Locate and identify every blood parasite.
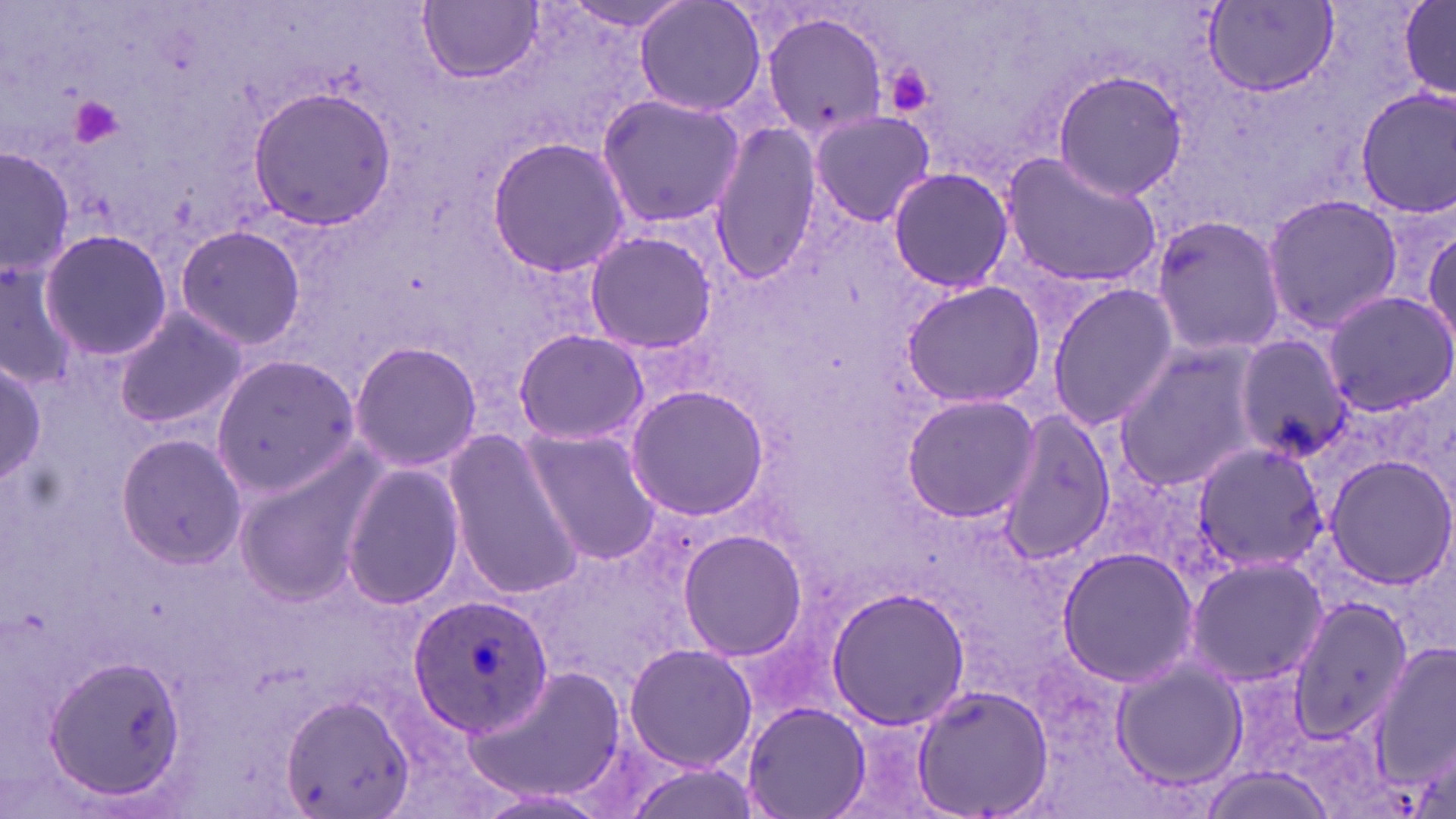

Approximate bounding boxes as (x1,y1)-(x2,y2) corner pairs in pixels.
Plasmodium ovale-infected red blood cells: (410,593)-(554,736).
No Plasmodium falciparum, Plasmodium malariae, Plasmodium vivax, Babesia divergens, or Trypanosoma brucei observed.

slide-level diagnosis = Plasmodium ovale
uninfected red blood cell locations = approximate bounding boxes as (x1,y1)-(x2,y2) corner pairs in pixels: (632,0)-(768,118), (1397,0)-(1455,103), (420,1)-(542,84), (1201,2)-(1338,98), (756,8)-(889,143), (1050,68)-(1188,201), (245,85)-(398,230), (1356,88)-(1456,218), (596,95)-(746,228), (807,108)-(938,229), (710,122)-(822,282), (486,135)-(630,278), (1,145)-(75,285), (998,151)-(1164,289), (886,167)-(1015,294), (1262,192)-(1402,335), (1149,213)-(1286,359), (172,224)-(306,350), (1424,225)-(1456,348), (583,227)-(719,355), (37,229)-(172,361), (0,262)-(79,391), (901,279)-(1047,409), (1047,283)-(1176,431), (1322,290)-(1456,415), (112,306)-(246,428), (513,327)-(648,448), (1232,337)-(1352,462), (348,340)-(483,471), (1111,345)-(1264,492), (210,355)-(359,493), (0,360)-(48,483), (627,383)-(771,521), (901,392)-(1043,522), (990,412)-(1116,564), (523,426)-(666,568), (445,430)-(586,600), (114,431)-(247,568), (1194,442)-(1328,575), (1323,454)-(1456,589), (232,456)-(375,605), (339,460)-(467,613), (678,530)-(807,660), (1058,547)-(1201,687), (1186,555)-(1326,686), (825,586)-(972,730), (1286,597)-(1413,742), (1376,639)-(1456,797), (624,642)-(757,774), (45,653)-(188,802), (1109,658)-(1247,790), (910,682)-(1057,819), (280,694)-(415,819), (744,703)-(868,818)
preparation = thin blood smear
image size = 1456×819 pixels
magnification = 1000x
platelet locations = approximate bounding boxes as (x1,y1)-(x2,y2) corner pairs in pixels: (884,64)-(937,121), (68,95)-(128,152)
modality = light microscopy
field of view = one of a larger specimen
stain = May-Grünwald-Giemsa